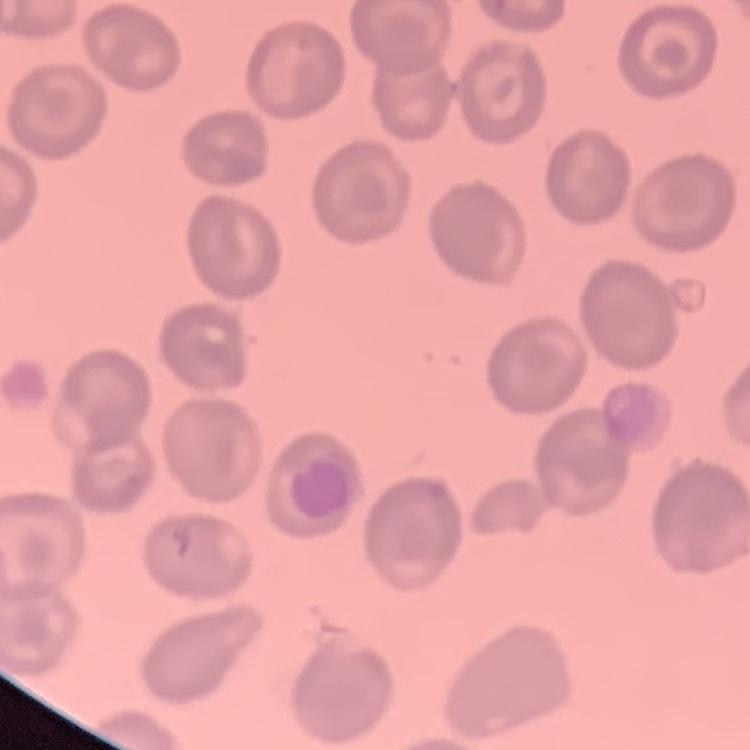
Summary:
  - Red blood cell morphology: no rouleaux formation
  - Preparation: thin blood film
  - Image type: one tile cut from a larger photomicrograph
  - Stain: Field's or Giemsa